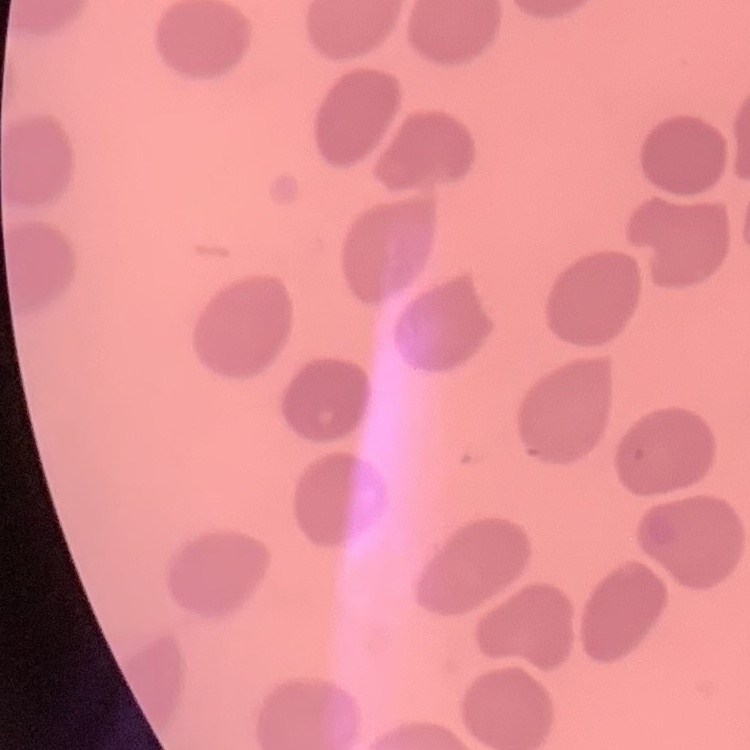

erythrocyte_morphology: no rouleaux formation
stain: Field's or Giemsa
image_type: one tile cut from a larger photomicrograph
preparation: thin blood film